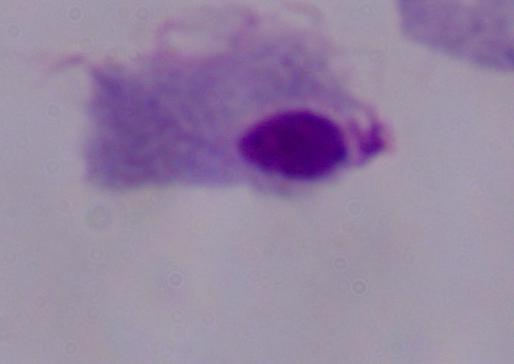
magnification = 1000x
modality = photomicrograph
identification = trichomonad